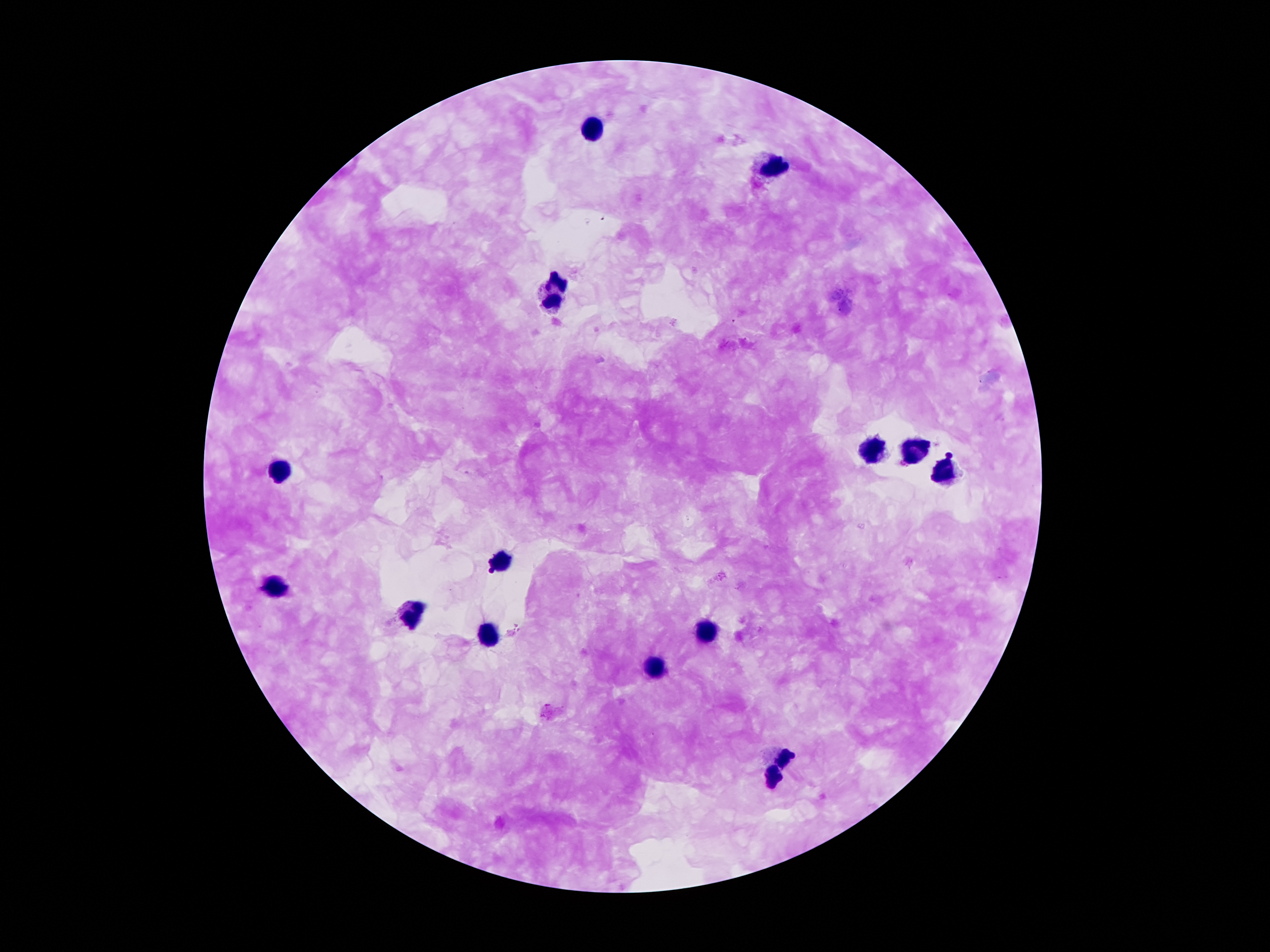
Approximate centers as (x, y) in pixels. Leukocyte locations: (596, 130), (777, 164), (557, 291), (873, 450), (913, 453), (284, 469), (943, 472), (499, 563), (272, 591), (408, 612), (708, 630), (486, 634), (658, 670), (785, 761), (772, 774). Patient malaria status: infected with Plasmodium falciparum. One field from this slide. Giemsa-stained preparation. 100x magnification. Plasmodium parasites: not seen. Thick blood film. Image is 1270×952 pixels. Photographed through the microscope eyepiece with a smartphone camera.